Assess this cell for malaria.
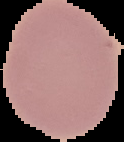
Uninfected.

image_size: 124×142 pixels
preparation: thin blood smear
image_type: segmented cell region with the area outside set to black